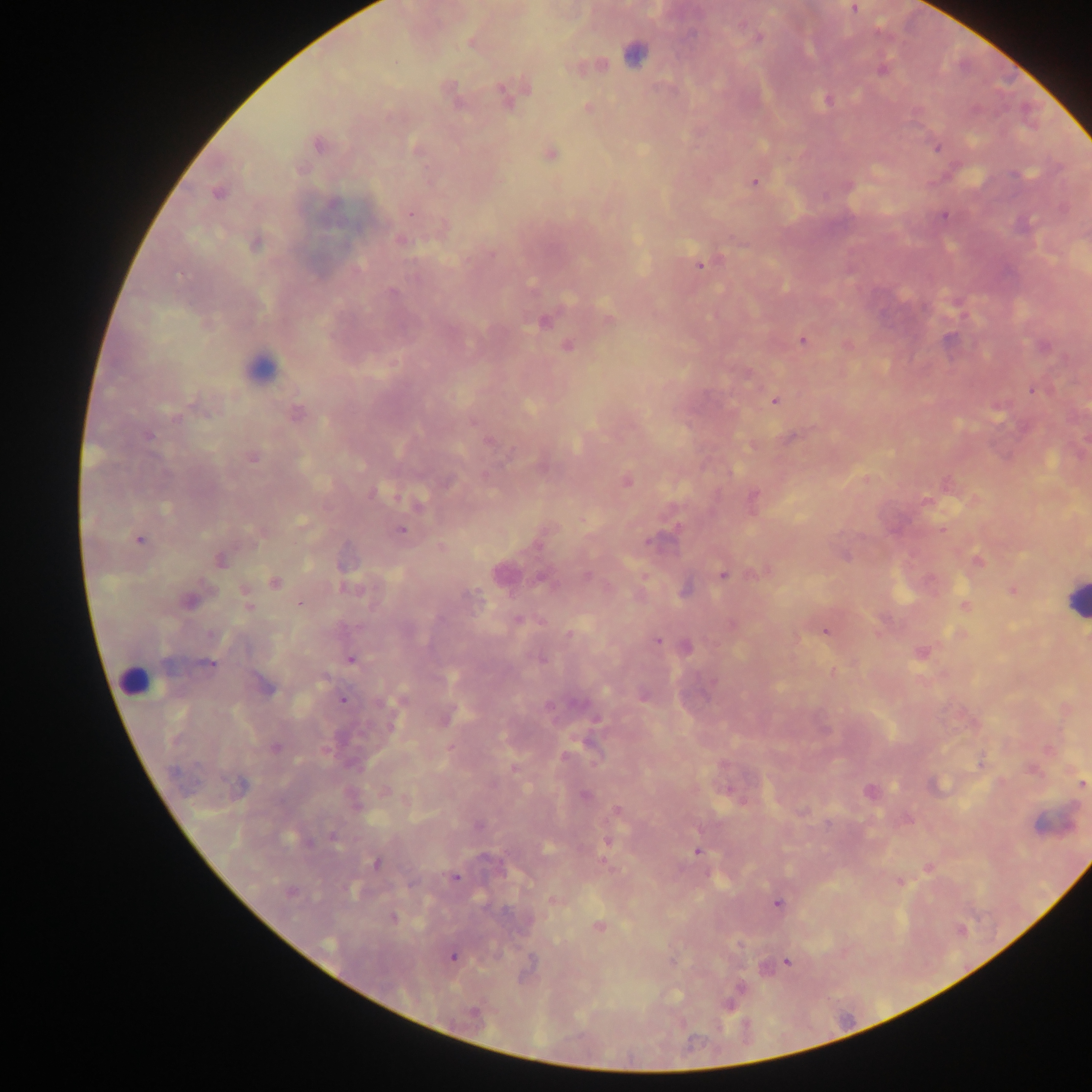
image_size: 1092×1092 pixels
field_of_view: single
plasmodium_parasite_locations: 'approximate centers as x y in pixels: 855 8; 471 42; 634 54; 882 70; 507 94; 827 100; 588 108; 319 146; 938 148; 550 155; 754 183; 218 193; 333 203; 410 213; 944 216; 400 240; 255 244; 700 265; 392 292; 544 321; 608 321; 802 340; 567 347; 1032 391; 775 401; 297 413; 177 417; 474 422; 148 436; 489 442; 252 458; 447 482; 627 482; 372 493; 753 497; 165 509; 302 521; 400 530; 140 539; 649 541; 844 555; 220 560; 978 560; 502 573; 722 574; 587 576; 541 578; 274 582; 685 590; 1013 591; 471 596; 190 600; 300 604; 248 605; 965 606; 518 621; 825 631; 570 634; 210 635; 657 641; 687 647; 352 659; 540 659; 208 664; 264 685; 343 700; 276 747; 980 765; 1081 784; 239 785; 870 791; 586 795; 478 825; 335 837; 309 842; 607 842; 697 852; 376 863; 454 878; 291 892; 778 903; 393 918; 599 926; 328 944; 453 957; 788 963; 740 988'
country: Ghana
capture: mobile-phone photograph through a microscope
preparation: thick blood film
leukocyte_locations: 'approximate centers as x y in pixels: 259 367; 1074 598; 133 680'